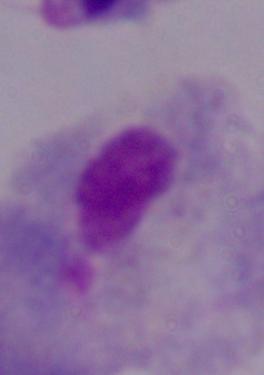
A trichomonad is shown. 1000x magnification. Photomicrograph.